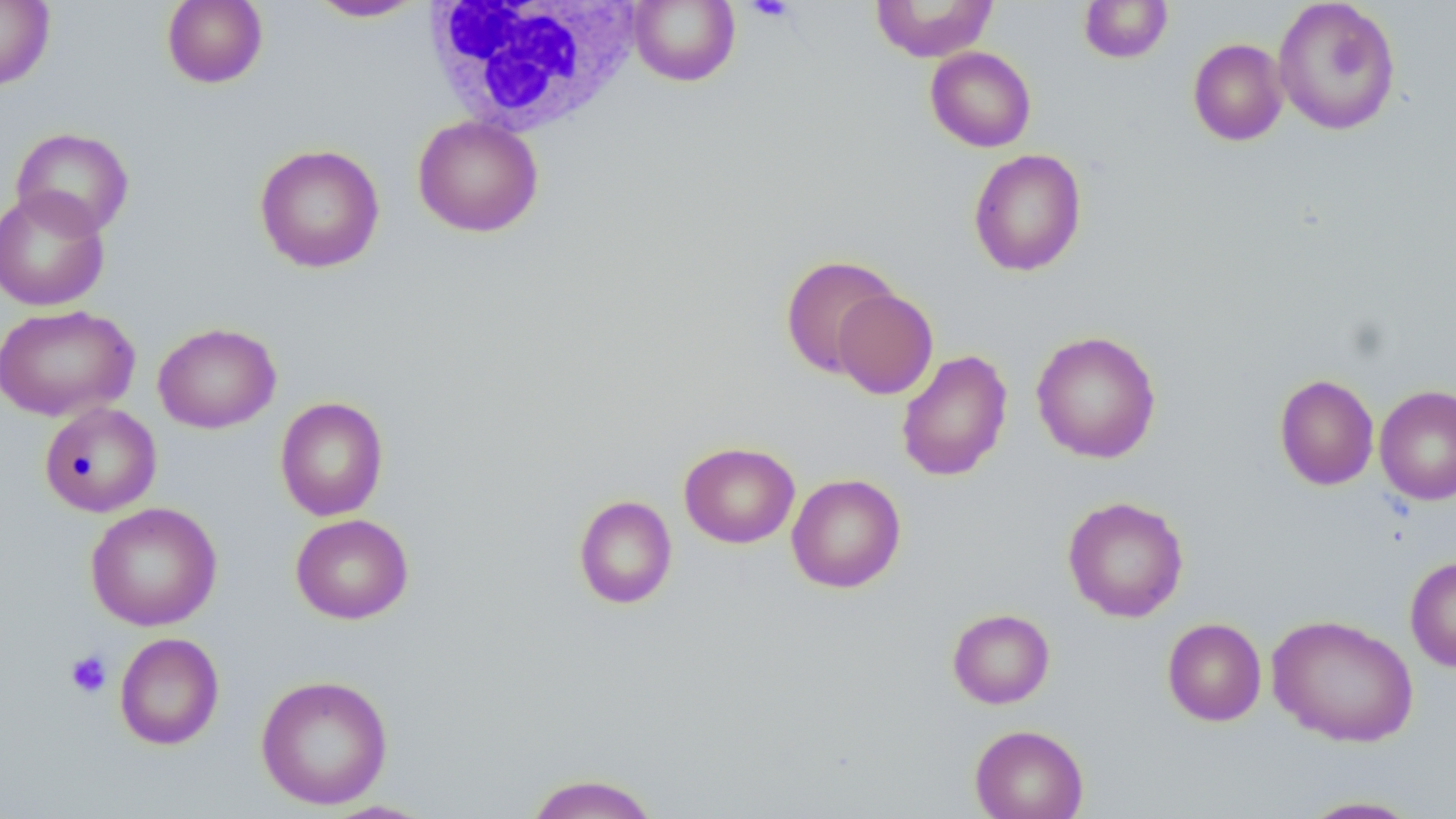
Summary:
  - Coordinate format: approximate bounding boxes as (x1, y1, x2, y2) in pixels
  - Uninfected red blood cell locations: (0, 0, 55, 89), (161, 0, 268, 88), (629, 0, 740, 86), (870, 0, 999, 62), (1079, 0, 1172, 64), (1273, 0, 1402, 135), (306, 1, 427, 22), (1188, 38, 1288, 146), (925, 46, 1036, 152), (412, 115, 543, 237), (11, 127, 134, 238), (254, 143, 385, 273), (968, 148, 1087, 277), (0, 187, 111, 311), (779, 253, 901, 378), (832, 288, 938, 399), (0, 304, 139, 422), (153, 322, 281, 433), (1031, 331, 1162, 463), (896, 348, 1013, 482), (1274, 373, 1379, 490), (1374, 385, 1456, 505), (275, 396, 388, 520), (39, 402, 162, 517), (679, 441, 800, 548), (786, 473, 906, 593), (573, 494, 677, 609), (1062, 496, 1189, 622), (85, 501, 222, 631), (290, 513, 414, 624), (1405, 556, 1456, 672), (947, 608, 1055, 708), (1267, 614, 1419, 747), (1162, 617, 1267, 726), (114, 632, 224, 750), (255, 674, 394, 809), (969, 724, 1088, 819), (524, 772, 660, 818), (1294, 795, 1428, 818)
  - Platelet locations: (744, 0, 797, 22), (65, 649, 113, 699)
  - White blood cell locations: (423, 0, 639, 139)
  - Slide-level diagnosis: negative for blood parasites
  - Preparation: thin blood smear
  - Field of view: one of a larger specimen
  - Stain: May-Grünwald-Giemsa
  - Magnification: 1000x
  - Modality: optical microscopy
  - Image size: 1456×819 pixels